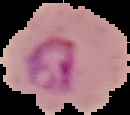
result: malaria parasites identified
image_type: segmented cell region with the area outside set to black
preparation: thin blood smear
image_size: 130×115 pixels